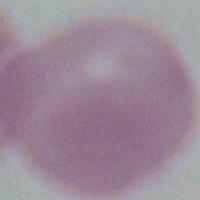

modality: micrograph
identification: red blood cell
magnification: 1000x